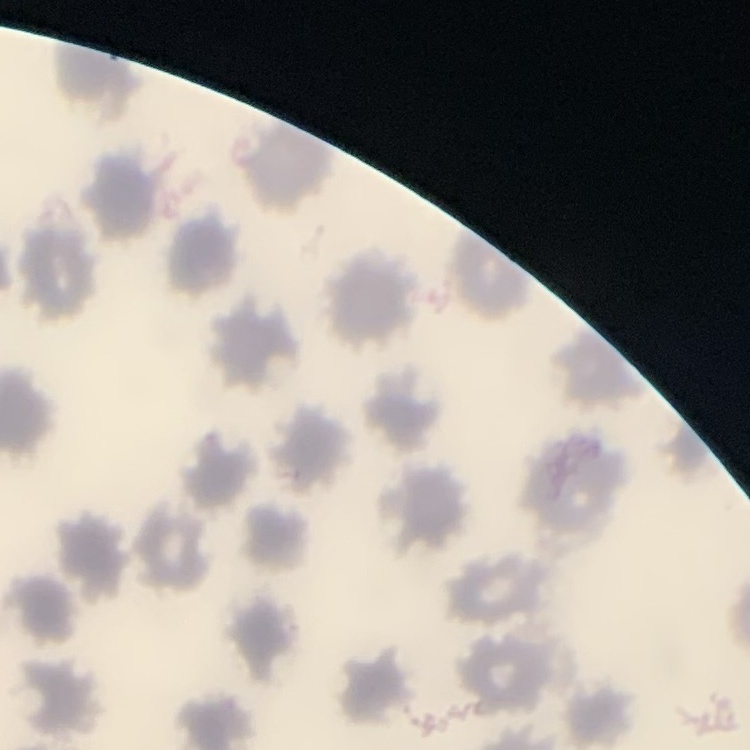

The red blood cells exhibit no rouleaux formation. Thin blood smear. Square crop of a larger photomicrograph. Field's or Giemsa stain.